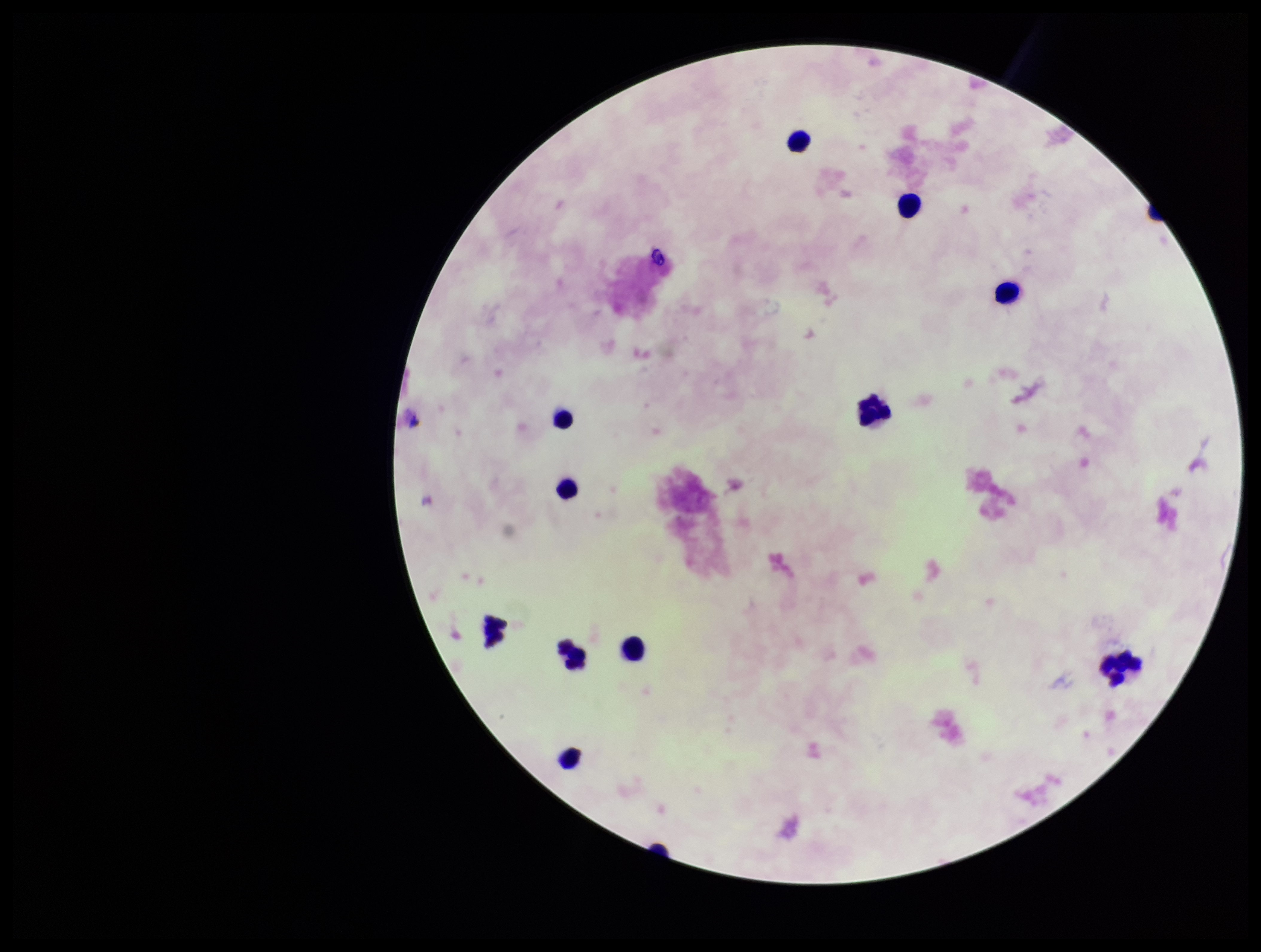
patient malaria status = negative
leukocyte count = 11
parasite count = 0
preparation = thick
stain = Giemsa
Plasmodium parasites = none identified
capture = smartphone photograph through the microscope eyepiece
image size = 1261×952 pixels
field of view = one from this slide